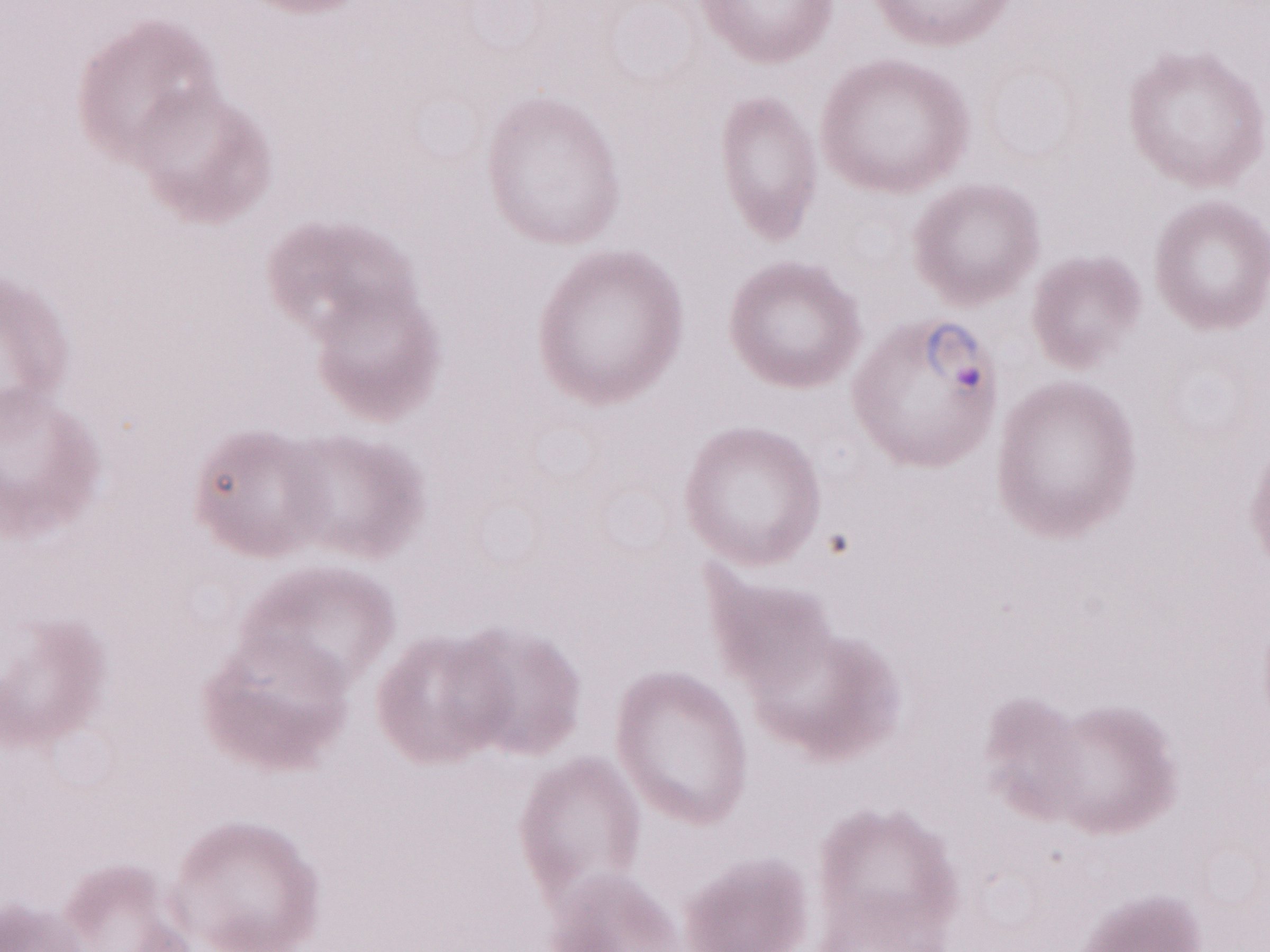

Olympus BX43 microscope, Olympus DP73 camera. 1,000x magnification. Malaria diagnosis (patient-level): positive. Thin blood film. May-Grünwald-Giemsa-stained preparation. Single field of view. Image is 1270×952 pixels.